Name the parasite shown.
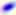
Toxoplasma gondii.

magnification = 400x
modality = micrograph